Describe the morphology of the erythrocytes.
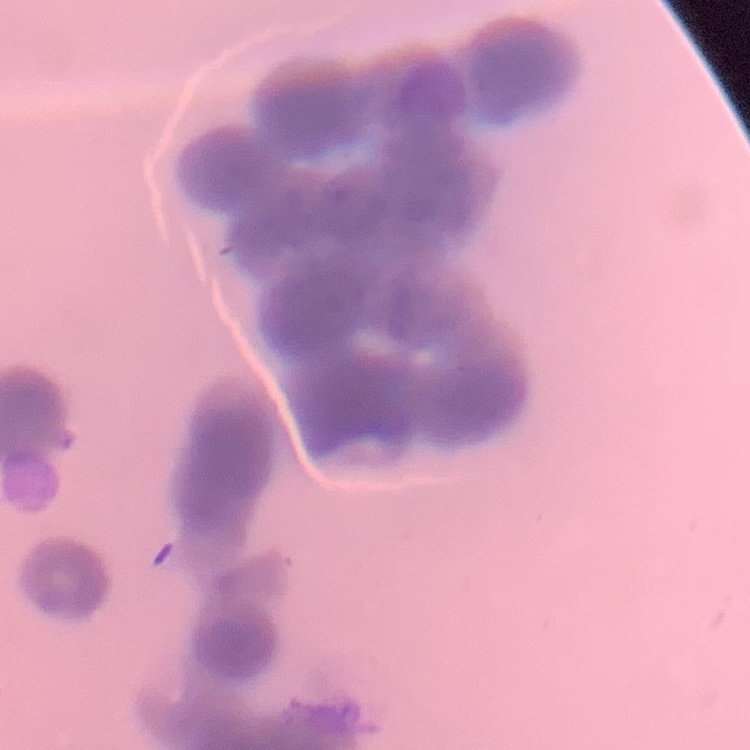

They show rouleaux formation.

Field's or Giemsa stain. One tile cut from a larger photomicrograph. Thin blood film.